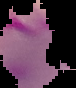
Summary:
  - Image type: segmented cell region on a black background
  - Preparation: thin blood smear
  - Malaria status: parasitized
  - Image size: 76×88 pixels